Assess the morphology of the erythrocytes.
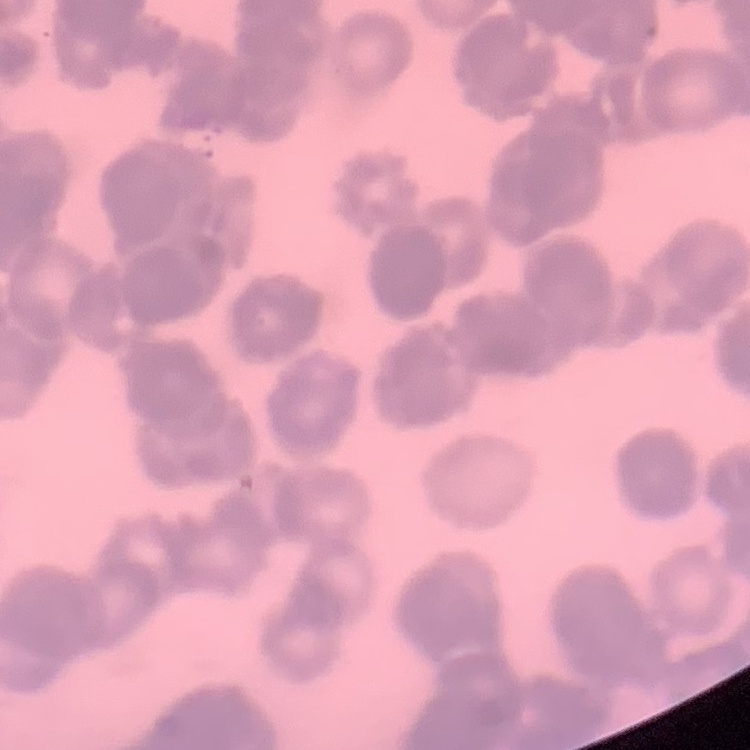

Rouleaux formation.

Field's or Giemsa stain. Square crop of a larger photomicrograph. Thin blood film.